Outline platelets.
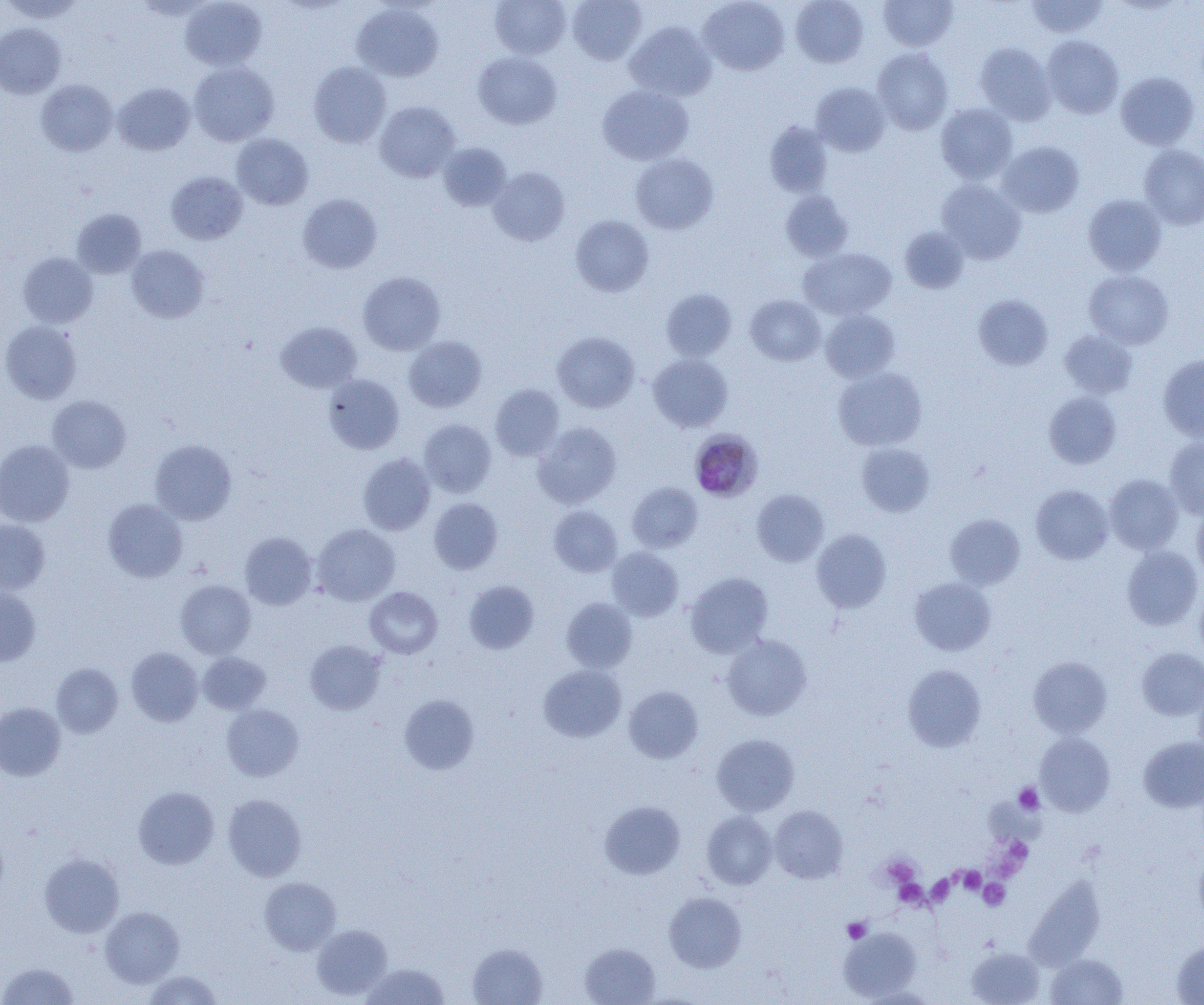
Approximate bounding boxes as named x1/y1/x2/y2 corners in pixels.
Platelets: (x1=1014, y1=783, x2=1044, y2=814), (x1=998, y1=835, x2=1033, y2=874), (x1=882, y1=856, x2=920, y2=889), (x1=957, y1=866, x2=985, y2=895), (x1=926, y1=874, x2=956, y2=906), (x1=894, y1=878, x2=927, y2=909), (x1=979, y1=879, x2=1010, y2=910), (x1=843, y1=918, x2=870, y2=943).

slide_level_diagnosis: Plasmodium malariae
field_of_view: single
modality: optical microscopy
plasmodium_malariae_infected_red_blood_cell_locations: 'approximate bounding boxes as named x1/y1/x2/y2 corners in pixels: (x1=690, y1=431, x2=760, y2=500)'
magnification: 1000x
preparation: thin blood film
image_size: 1204×1005 pixels
uninfected_red_blood_cell_locations: 'approximate bounding boxes as named x1/y1/x2/y2 corners in pixels: (x1=1, y1=0, x2=86, y2=23), (x1=490, y1=0, x2=571, y2=59), (x1=567, y1=0, x2=647, y2=64), (x1=699, y1=0, x2=789, y2=75), (x1=791, y1=0, x2=869, y2=68), (x1=878, y1=0, x2=958, y2=51), (x1=1025, y1=0, x2=1108, y2=39), (x1=180, y1=1, x2=267, y2=70), (x1=351, y1=3, x2=443, y2=82), (x1=624, y1=21, x2=716, y2=102), (x1=0, y1=23, x2=66, y2=99), (x1=1042, y1=36, x2=1124, y2=118), (x1=975, y1=43, x2=1056, y2=125), (x1=872, y1=48, x2=954, y2=135), (x1=473, y1=51, x2=561, y2=129), (x1=188, y1=62, x2=279, y2=146), (x1=308, y1=62, x2=391, y2=148), (x1=1115, y1=72, x2=1199, y2=150), (x1=35, y1=79, x2=118, y2=156), (x1=113, y1=82, x2=195, y2=155), (x1=811, y1=82, x2=891, y2=156), (x1=597, y1=86, x2=693, y2=165), (x1=374, y1=101, x2=460, y2=182), (x1=936, y1=104, x2=1018, y2=184), (x1=764, y1=122, x2=833, y2=197), (x1=232, y1=134, x2=313, y2=210), (x1=997, y1=141, x2=1084, y2=218), (x1=438, y1=142, x2=511, y2=211), (x1=1139, y1=145, x2=1204, y2=230), (x1=631, y1=153, x2=719, y2=234), (x1=488, y1=167, x2=570, y2=246), (x1=166, y1=171, x2=247, y2=244), (x1=936, y1=178, x2=1026, y2=264), (x1=781, y1=190, x2=853, y2=261), (x1=298, y1=194, x2=382, y2=273), (x1=1083, y1=194, x2=1166, y2=276), (x1=71, y1=208, x2=146, y2=278), (x1=571, y1=215, x2=654, y2=297), (x1=899, y1=226, x2=969, y2=293), (x1=126, y1=245, x2=209, y2=323), (x1=798, y1=247, x2=896, y2=320), (x1=18, y1=253, x2=97, y2=328), (x1=1084, y1=270, x2=1174, y2=349), (x1=358, y1=272, x2=445, y2=355), (x1=661, y1=289, x2=737, y2=361), (x1=973, y1=294, x2=1054, y2=370), (x1=745, y1=295, x2=825, y2=365), (x1=820, y1=309, x2=900, y2=382), (x1=0, y1=320, x2=82, y2=404), (x1=276, y1=321, x2=362, y2=393), (x1=1059, y1=330, x2=1137, y2=399), (x1=552, y1=331, x2=640, y2=413), (x1=404, y1=336, x2=486, y2=412), (x1=648, y1=353, x2=733, y2=432), (x1=1158, y1=354, x2=1204, y2=441), (x1=833, y1=367, x2=927, y2=451), (x1=323, y1=374, x2=404, y2=454), (x1=491, y1=384, x2=564, y2=461), (x1=1044, y1=391, x2=1121, y2=468), (x1=48, y1=395, x2=131, y2=473), (x1=418, y1=419, x2=496, y2=497), (x1=533, y1=422, x2=622, y2=508), (x1=1165, y1=437, x2=1204, y2=518), (x1=150, y1=439, x2=237, y2=525), (x1=0, y1=440, x2=74, y2=526), (x1=857, y1=442, x2=935, y2=517), (x1=358, y1=453, x2=435, y2=535), (x1=1105, y1=474, x2=1183, y2=554), (x1=627, y1=482, x2=703, y2=553), (x1=1031, y1=484, x2=1112, y2=564), (x1=752, y1=489, x2=829, y2=566), (x1=429, y1=498, x2=503, y2=574), (x1=103, y1=499, x2=187, y2=582), (x1=1191, y1=503, x2=1204, y2=582), (x1=549, y1=505, x2=622, y2=577), (x1=946, y1=514, x2=1025, y2=589), (x1=0, y1=519, x2=50, y2=595), (x1=313, y1=524, x2=400, y2=606), (x1=812, y1=530, x2=892, y2=612), (x1=240, y1=532, x2=317, y2=610), (x1=1122, y1=546, x2=1203, y2=630), (x1=607, y1=547, x2=683, y2=621), (x1=685, y1=572, x2=773, y2=657), (x1=909, y1=576, x2=997, y2=656), (x1=175, y1=579, x2=256, y2=658), (x1=464, y1=581, x2=539, y2=654), (x1=0, y1=586, x2=41, y2=666), (x1=364, y1=586, x2=442, y2=658), (x1=1194, y1=587, x2=1204, y2=661), (x1=562, y1=598, x2=637, y2=673), (x1=722, y1=634, x2=812, y2=721), (x1=305, y1=640, x2=386, y2=715), (x1=126, y1=647, x2=203, y2=726), (x1=1136, y1=648, x2=1204, y2=720), (x1=198, y1=652, x2=271, y2=714), (x1=1028, y1=656, x2=1112, y2=737), (x1=51, y1=663, x2=123, y2=738), (x1=902, y1=664, x2=986, y2=752), (x1=538, y1=665, x2=626, y2=742), (x1=1194, y1=681, x2=1204, y2=760), (x1=624, y1=686, x2=703, y2=763), (x1=399, y1=694, x2=479, y2=775), (x1=0, y1=702, x2=65, y2=781), (x1=222, y1=704, x2=304, y2=781), (x1=1035, y1=732, x2=1115, y2=816), (x1=712, y1=734, x2=799, y2=816), (x1=1138, y1=736, x2=1204, y2=813), (x1=133, y1=786, x2=219, y2=869), (x1=223, y1=794, x2=306, y2=881), (x1=600, y1=801, x2=685, y2=880), (x1=769, y1=805, x2=848, y2=883), (x1=702, y1=811, x2=777, y2=889), (x1=1194, y1=850, x2=1204, y2=927), (x1=39, y1=854, x2=124, y2=937), (x1=259, y1=877, x2=341, y2=955), (x1=1028, y1=878, x2=1109, y2=974), (x1=664, y1=892, x2=747, y2=973), (x1=100, y1=906, x2=184, y2=987), (x1=311, y1=924, x2=393, y2=1000), (x1=839, y1=926, x2=922, y2=1001), (x1=1171, y1=939, x2=1204, y2=1004), (x1=467, y1=943, x2=548, y2=1005), (x1=580, y1=943, x2=660, y2=1005), (x1=966, y1=946, x2=1044, y2=1005), (x1=1046, y1=953, x2=1128, y2=1004), (x1=0, y1=962, x2=79, y2=1005), (x1=362, y1=964, x2=449, y2=1005), (x1=143, y1=970, x2=223, y2=1004), (x1=857, y1=986, x2=938, y2=1004)'